Name the cell type shown.
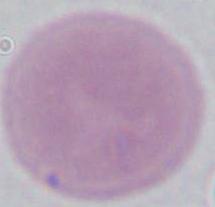

An erythrocyte.

Summary:
  - Magnification: 1000x
  - Modality: micrograph